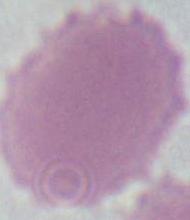 Micrograph. A red blood cell is shown. Captured at 1000x magnification.